Locate every Plasmodium parasite.
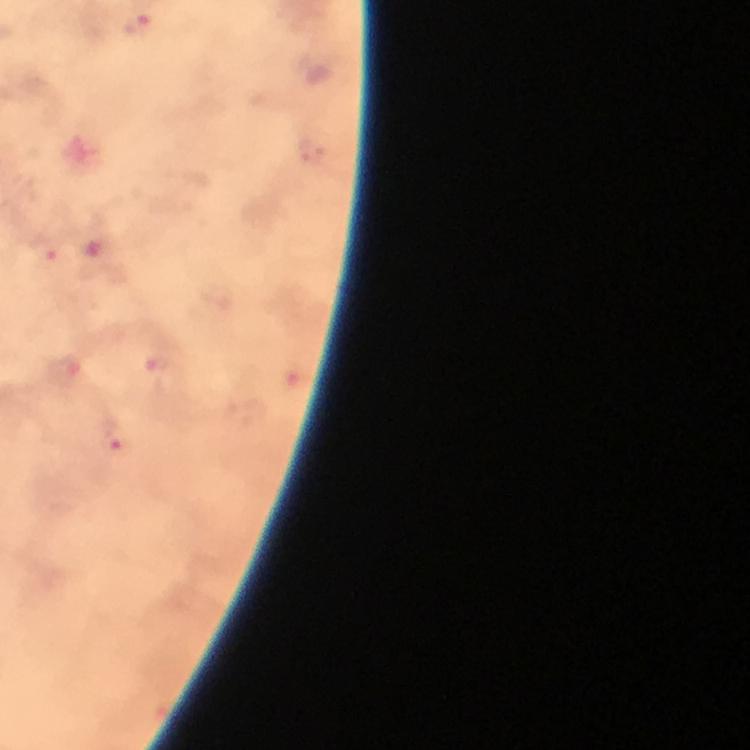
Approximate centers as (x, y) in pixels.
Plasmodium parasites: (139, 23), (44, 253), (165, 373), (116, 441).

From a diagnostic examination for malaria. 100x magnification. Photographed through the microscope with a smartphone camera. Thick blood smear. Giemsa stain. Immersion oil applied. Cropped region of a single field of view. Image is 750×750 pixels.